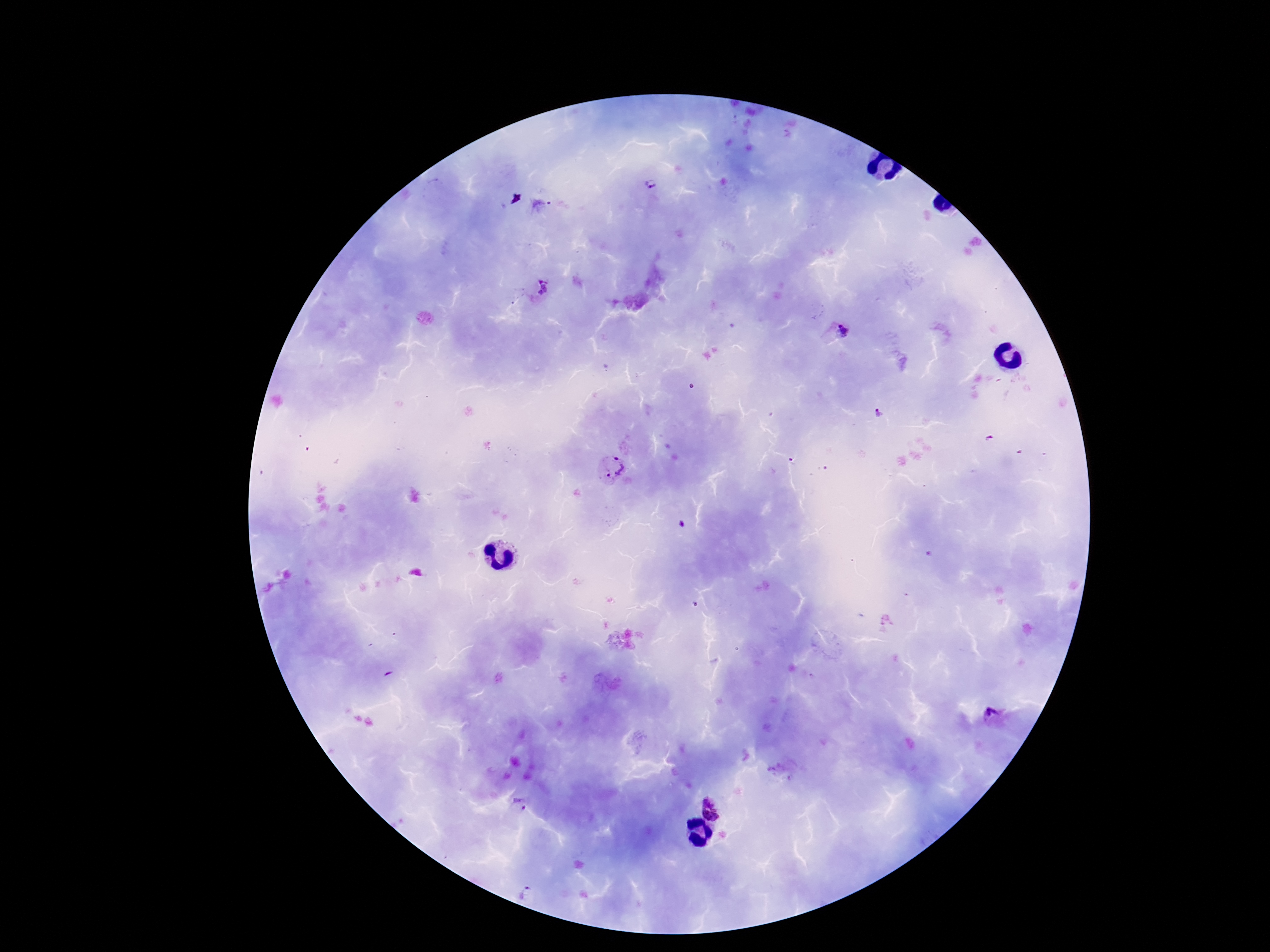

Approximate centers as {x, y} in pixels. Plasmodium parasite locations: {650, 184}, {544, 287}, {842, 332}, {879, 413}, {990, 439}, {613, 468}, {993, 717}, {720, 800}, {519, 806}, {527, 891}. Image is 1270×952 pixels. Photographed through the microscope eyepiece with a smartphone camera. Patient malaria status: infected. Thick peripheral-blood smear. Giemsa-stained preparation. One field from this slide. 100x magnification.